Classify this cell by malaria status.
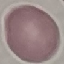

It is uninfected.

stain = Giemsa
capture = smartphone camera at the microscope eyepiece
image type = cell patch, automatically extracted from a larger field of view and resized to 64 × 64 pixels
preparation = thin blood smear